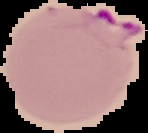
preparation = thin blood film
image type = segmented cell region with the area outside set to black
malaria status = parasitized
image size = 148×133 pixels